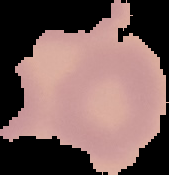
From a thin blood film. Result: negative for malaria parasites. Image is 169×175 pixels. Cell region segmented out of the field of view; the surrounding area is masked to black.